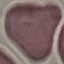 Malaria status: uninfected. Giemsa-stained preparation. Acquired by smartphone through the microscope eyepiece. Thin blood smear. Cell patch, automatically extracted from a larger field of view and resized to 64 × 64 pixels.